Comment on the morphology of the erythrocytes.
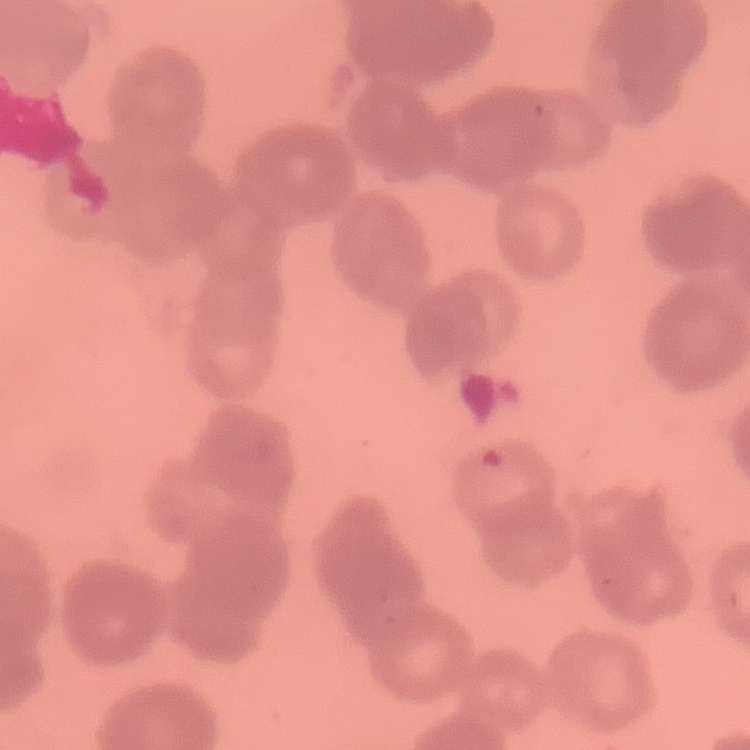

Rouleaux formation.

Summary:
  - Image type: one tile cut from a larger photomicrograph
  - Preparation: thin peripheral smear
  - Stain: Field's or Giemsa